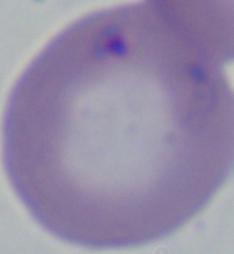

Summary:
  - Modality: micrograph
  - Identification: Babesia
  - Magnification: 1000x